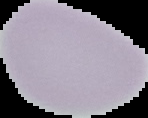
Image is 148×118 pixels. From a thin blood smear. Malaria status: uninfected. Segmented cell region on a black background.